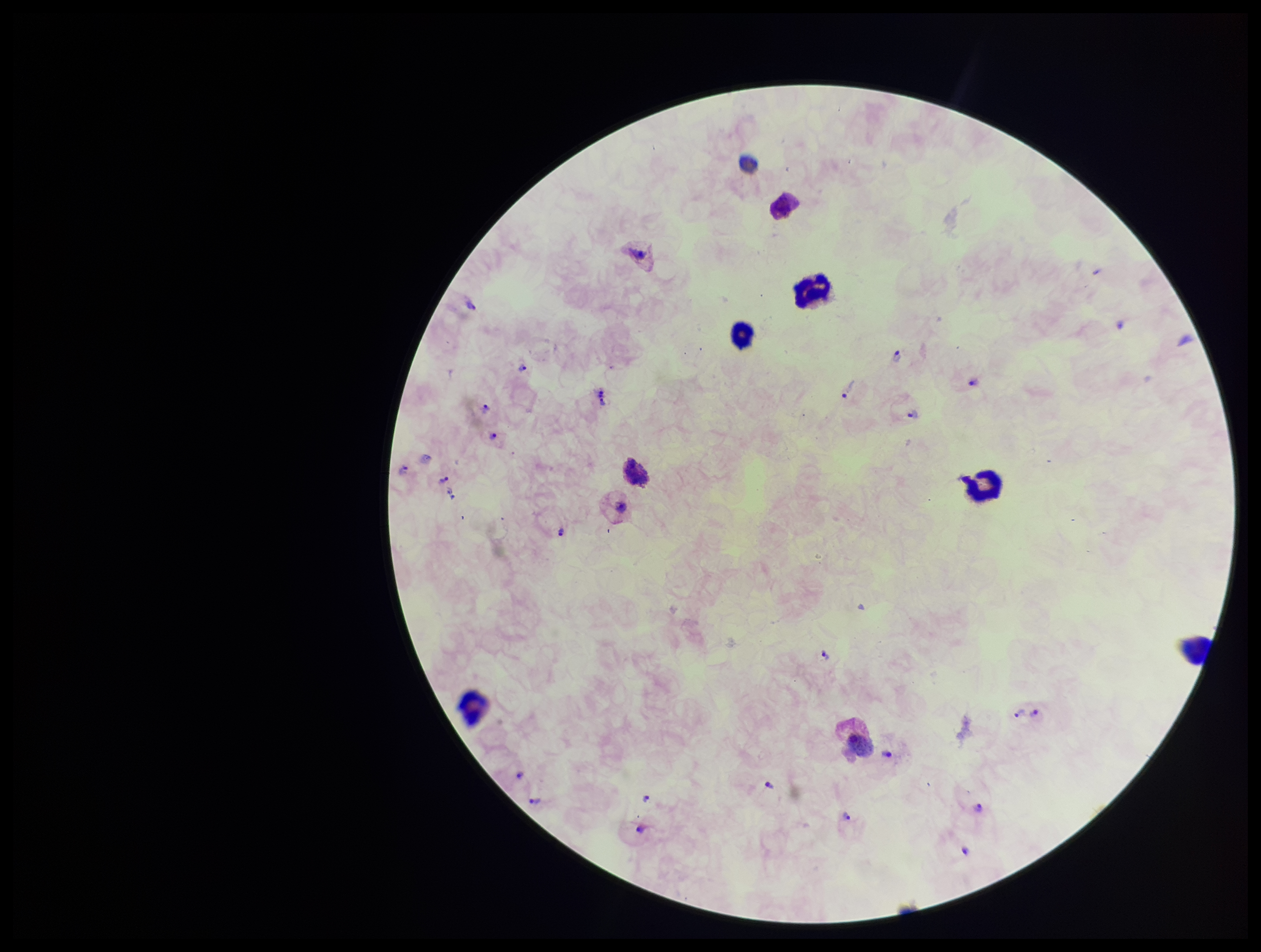

Summary:
  - Stain: Giemsa
  - Parasite count: 25
  - Capture: smartphone photograph through the microscope eyepiece
  - Field of view: single
  - Species reported for this patient: Plasmodium vivax
  - Patient malaria status: positive
  - Leukocyte count: 8
  - Image size: 1261×952 pixels
  - Preparation: thick
  - Plasmodium parasites: identified